Classify this cell by malaria status.
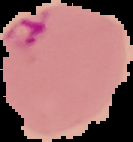

Parasitized.

image size = 133×142 pixels
image type = cell region segmented out of the field of view; surrounding area masked to black
preparation = thin blood smear